Locate and identify every blood parasite.
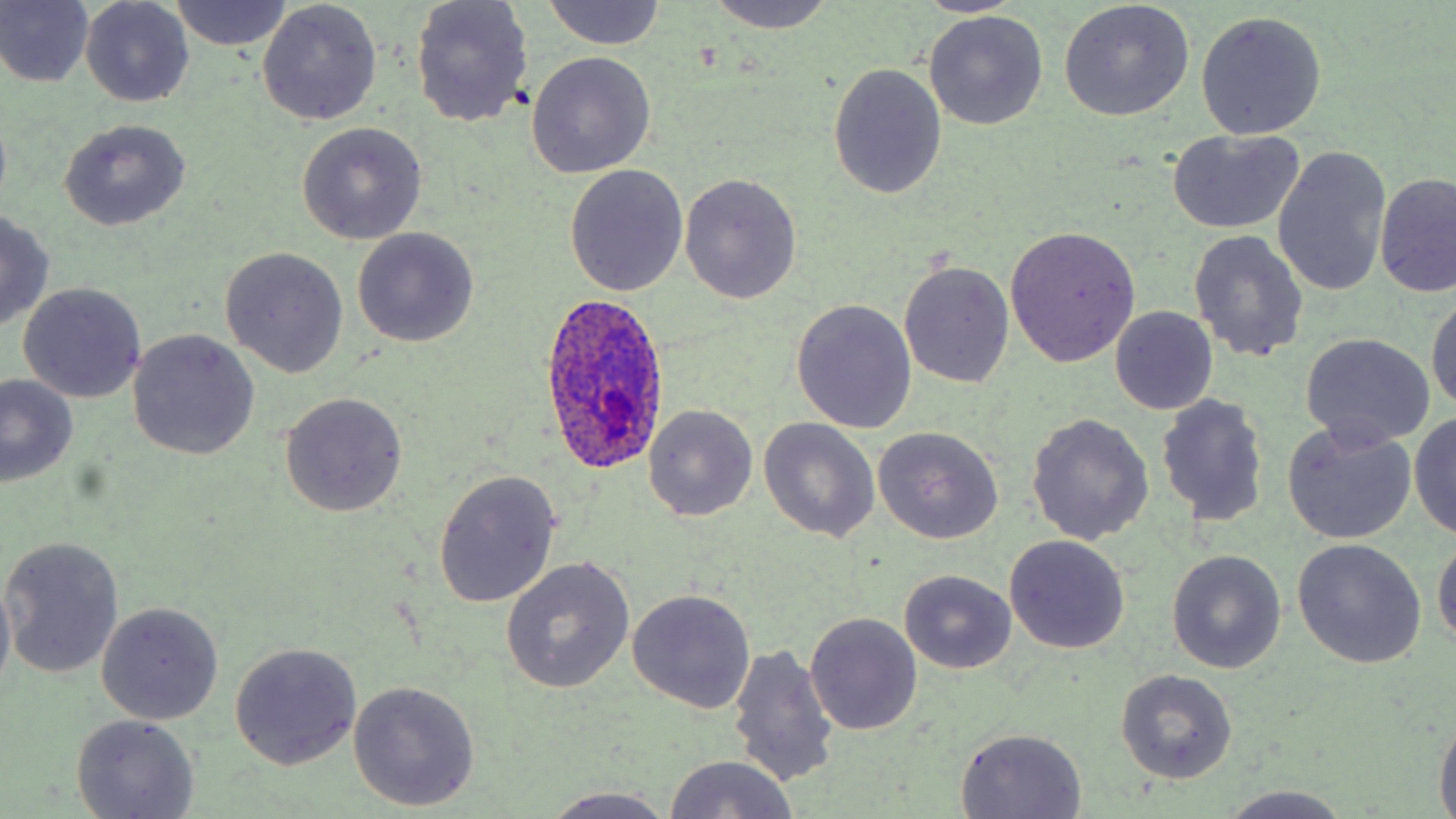
Approximate bounding boxes as (x1,y1)-(x2,y2) corner pairs in pixels.
Plasmodium ovale-infected red blood cells: (538,292)-(673,476).
No Plasmodium falciparum, Plasmodium malariae, Plasmodium vivax, Babesia divergens, or Trypanosoma brucei observed.

slide-level diagnosis = Plasmodium ovale
stain = May-Grünwald-Giemsa
uninfected red blood cell locations = approximate bounding boxes as (x1,y1)-(x2,y2) corner pairs in pixels: (0,0)-(94,88), (409,0)-(534,128), (703,0)-(839,35), (911,0)-(1026,16), (168,1)-(292,51), (543,1)-(666,51), (1059,1)-(1195,121), (80,2)-(194,108), (256,2)-(382,125), (924,10)-(1048,130), (1196,11)-(1326,139), (526,50)-(656,178), (827,64)-(948,199), (58,119)-(191,231), (296,121)-(427,245), (1166,127)-(1306,235), (1272,146)-(1391,298), (565,166)-(688,298), (679,173)-(802,304), (1376,173)-(1455,297), (0,210)-(54,329), (1004,226)-(1140,367), (351,229)-(478,348), (1187,229)-(1308,363), (221,247)-(349,378), (898,261)-(1015,389), (18,282)-(147,403), (1428,290)-(1456,415), (790,298)-(918,434), (1110,306)-(1218,416), (127,331)-(258,461), (1301,333)-(1435,449), (0,374)-(79,486), (279,391)-(407,518), (1155,393)-(1270,527), (644,405)-(758,521), (1411,410)-(1456,541), (1025,411)-(1154,547), (757,418)-(880,543), (1282,421)-(1417,544), (872,427)-(1004,545), (433,469)-(564,609), (1432,532)-(1455,656), (1,536)-(126,678), (1003,537)-(1129,655), (1291,539)-(1426,668), (1167,551)-(1287,673), (501,556)-(635,693), (898,569)-(1018,673), (0,572)-(15,701), (628,590)-(756,713), (95,603)-(224,724), (805,612)-(922,735), (229,641)-(363,771), (726,642)-(840,788), (1115,668)-(1238,783), (348,679)-(480,812), (71,714)-(201,819), (1432,720)-(1455,814), (954,727)-(1088,818), (660,754)-(802,819), (1213,785)-(1354,819), (535,789)-(688,818)
preparation = thin blood smear
magnification = 1000x
modality = light microscopy
field of view = one of a larger specimen
image size = 1456×819 pixels